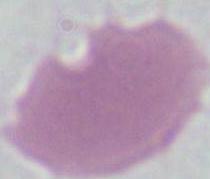 Photomicrograph. Captured at 1000x magnification. An erythrocyte is seen.